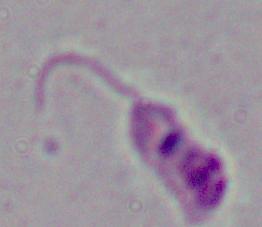
1000x magnification. A Leishmania parasite is shown. Micrograph.